Point out each Plasmodium parasite and each leukocyte.
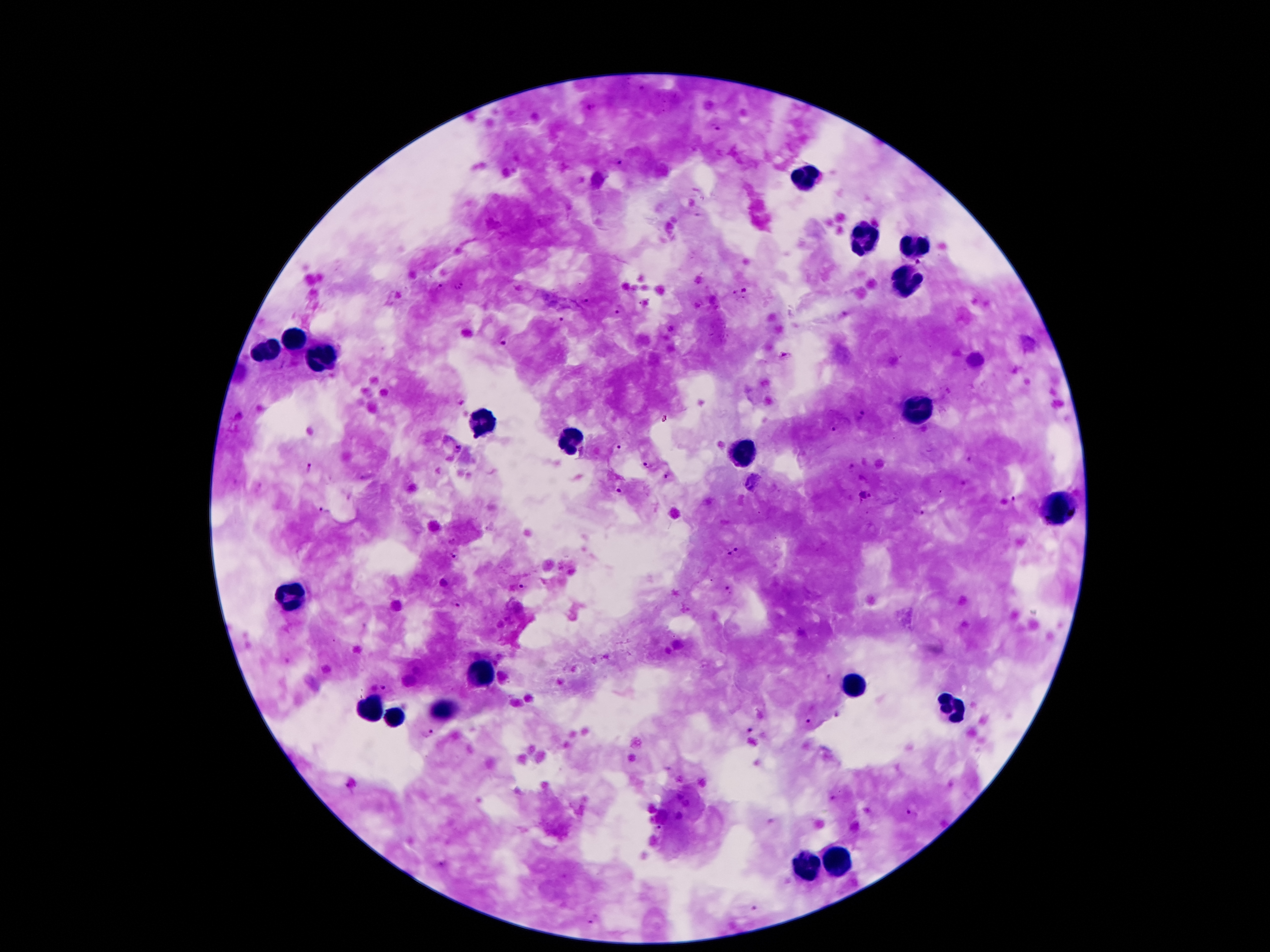

Approximate object centers, in pixels from the top-left corner.
Plasmodium parasites: (x=590, y=107), (x=718, y=128), (x=619, y=164), (x=919, y=261), (x=463, y=284), (x=441, y=288), (x=457, y=289), (x=744, y=290), (x=733, y=291), (x=587, y=300), (x=645, y=302), (x=617, y=311), (x=563, y=319), (x=503, y=341), (x=784, y=354), (x=862, y=415), (x=239, y=417), (x=834, y=431), (x=617, y=447), (x=458, y=450), (x=971, y=460), (x=310, y=466), (x=646, y=466), (x=667, y=477), (x=620, y=492), (x=864, y=497), (x=1015, y=500), (x=325, y=511), (x=918, y=512), (x=737, y=548), (x=455, y=555), (x=728, y=555), (x=520, y=588), (x=726, y=592), (x=456, y=603), (x=829, y=679), (x=385, y=687), (x=837, y=715), (x=807, y=721), (x=749, y=730), (x=427, y=734), (x=350, y=784), (x=833, y=800), (x=911, y=814), (x=658, y=829), (x=441, y=864), (x=754, y=908), (x=594, y=920).
Leukocytes: (x=805, y=179), (x=864, y=239), (x=913, y=244), (x=906, y=282), (x=295, y=342), (x=273, y=351), (x=327, y=356), (x=917, y=410), (x=483, y=424), (x=572, y=442), (x=742, y=450), (x=1060, y=508), (x=292, y=596), (x=479, y=672), (x=854, y=686), (x=952, y=707), (x=374, y=709), (x=449, y=711), (x=395, y=716), (x=834, y=861), (x=808, y=867).

Image is 1270×952 pixels. Patient malaria status: positive for Plasmodium falciparum. Giemsa stain. Thick blood smear. 100x magnification. One field from this slide. Photographed through the microscope eyepiece with a smartphone camera.